Comment on the morphology of the red blood cells.
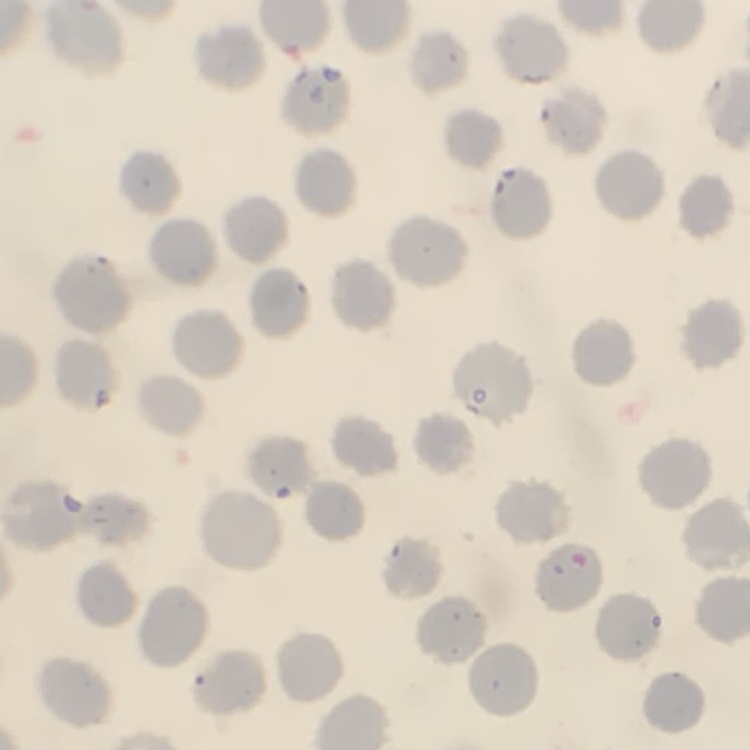

They show no rouleaux formation.

Summary:
  - Stain: Field's or Giemsa
  - Preparation: thin blood smear
  - Image type: one tile cut from a larger photomicrograph